Classify this cell by malaria status.
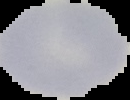

Uninfected.

Cell region segmented out of the field of view; the surrounding area is masked to black. Image is 130×100 pixels. From a thin blood film.